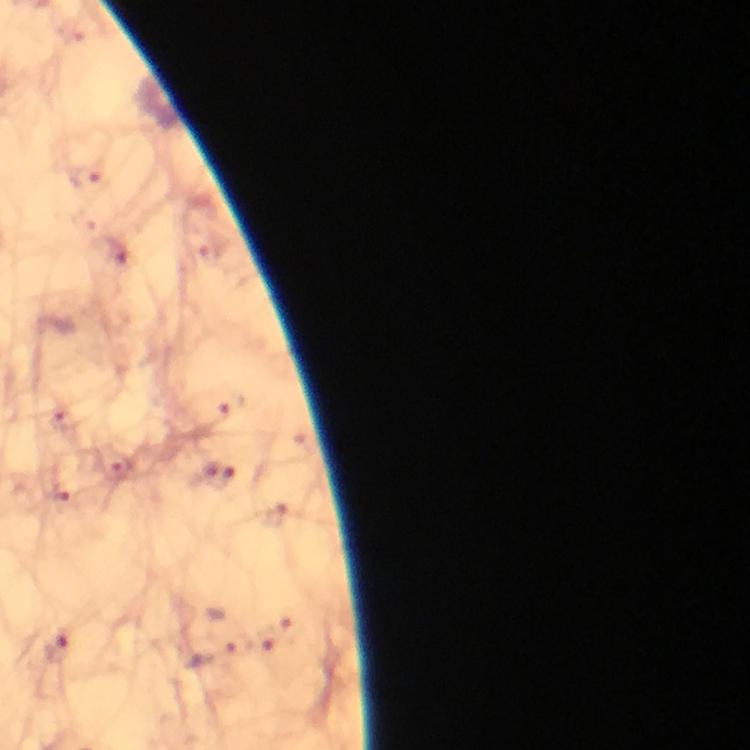
Approximate object centers, in pixels from the top-left corner.
Summary:
  - Malaria parasite locations: (x=217, y=475), (x=57, y=648)
  - Magnification: 100x
  - Cropped from: a single field of view
  - Context: from a malaria diagnostic workup
  - Stain: Giemsa
  - Preparation: thick blood film
  - Capture: smartphone photograph through a microscope
  - Immersion oil: used
  - Image size: 750×750 pixels